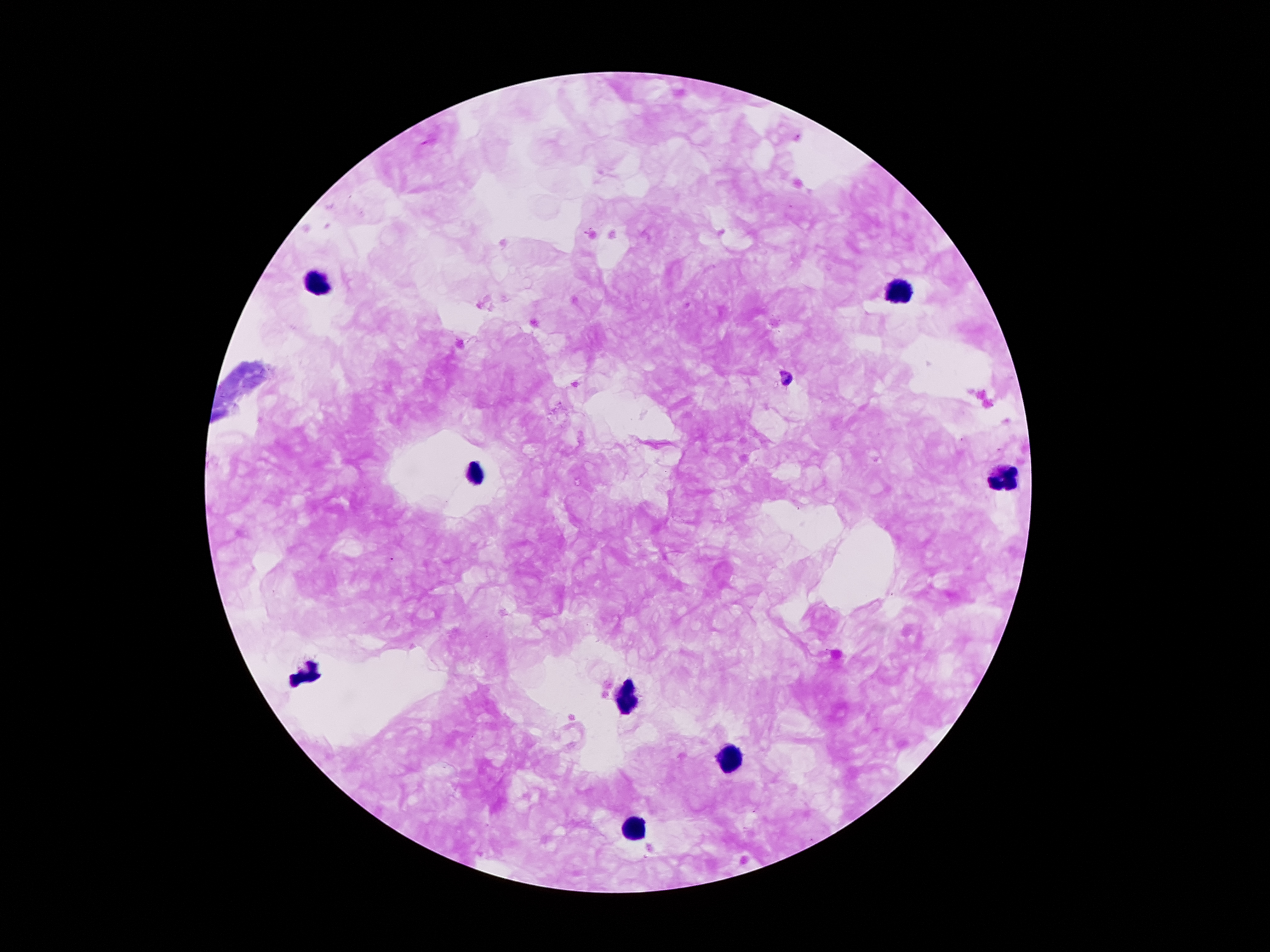
patient_malaria_status: positive for Plasmodium falciparum
capture: smartphone camera through the microscope eyepiece
field_of_view: single
malaria_parasite_locations: 'approximate centers as [x, y] in pixels: [786, 379]'
magnification: 100x
stain: Giemsa
leukocyte_locations: 'approximate centers as [x, y] in pixels: [323, 283], [896, 291], [474, 474], [1005, 474], [306, 675], [625, 700], [728, 758], [627, 832]'
preparation: thick peripheral-blood smear
image_size: 1270×952 pixels